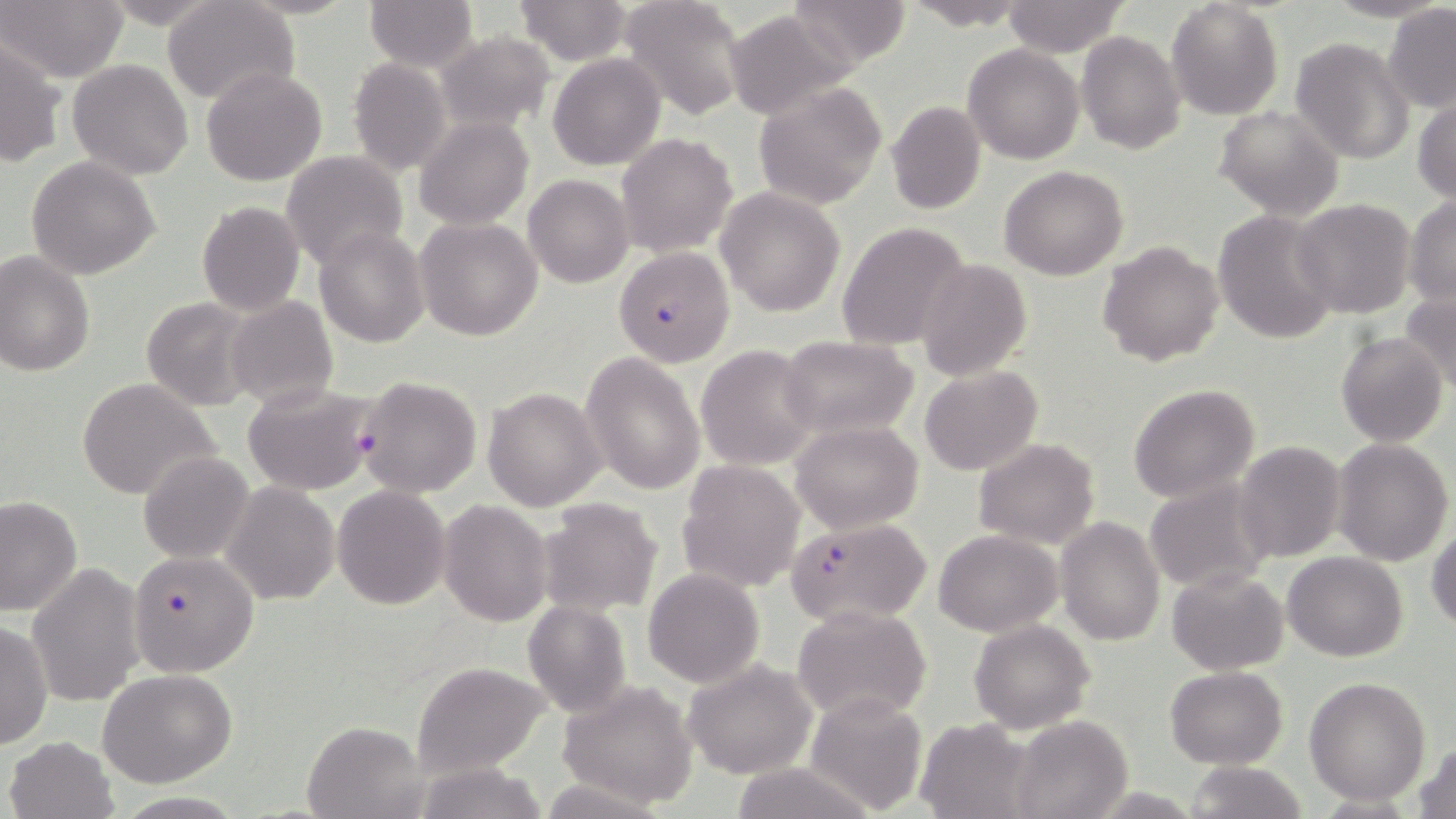

slide_level_diagnosis: Plasmodium falciparum
image_size: 1456×819 pixels
modality: optical microscopy
preparation: thin blood film
field_of_view: single
magnification: 1000x
plasmodium_falciparum_infected_red_blood_cell_locations: 'approximate bounding boxes as (x1,y1)-(x2,y2) corner pairs in pixels: (614,247)-(735,367), (357,375)-(484,498), (785,518)-(933,626), (127,549)-(259,677)'
stain: May-Grünwald-Giemsa
uninfected_red_blood_cell_locations: 'approximate bounding boxes as (x1,y1)-(x2,y2) corner pairs in pixels: (3,0)-(129,83), (98,0)-(225,28), (365,0)-(478,71), (620,0)-(748,120), (785,0)-(914,67), (901,0)-(1036,29), (163,1)-(297,106), (515,1)-(633,65), (1001,1)-(1130,56), (1166,2)-(1284,119), (1383,4)-(1456,111), (722,9)-(855,120), (1078,30)-(1187,155), (433,31)-(556,133), (2,35)-(67,169), (1290,37)-(1415,167), (962,45)-(1083,165), (547,54)-(666,170), (347,56)-(451,177), (67,59)-(193,179), (201,66)-(326,185), (754,82)-(887,210), (1413,93)-(1456,202), (885,101)-(986,216), (1215,104)-(1346,221), (414,116)-(534,231), (617,133)-(738,259), (281,151)-(408,270), (27,157)-(163,279), (999,165)-(1129,280), (523,174)-(633,288), (716,187)-(845,317), (1404,195)-(1456,308), (1292,200)-(1415,317), (196,204)-(303,316), (1212,208)-(1341,345), (414,217)-(543,340), (837,222)-(971,353), (314,226)-(428,348), (1097,241)-(1225,368), (0,250)-(96,376), (917,258)-(1031,382), (1399,290)-(1456,393), (225,295)-(338,410), (142,297)-(257,411), (1335,330)-(1448,447), (780,336)-(918,440), (697,344)-(820,471), (581,352)-(706,495), (919,365)-(1041,477), (76,377)-(221,500), (241,381)-(381,496), (1128,383)-(1259,503), (483,385)-(606,512), (792,420)-(922,532), (974,437)-(1098,549), (1234,438)-(1347,562), (1333,439)-(1453,568), (138,449)-(254,563), (677,460)-(805,593), (1140,476)-(1277,595), (223,483)-(339,604), (332,485)-(451,609), (537,496)-(663,617), (0,497)-(83,619), (439,499)-(552,626), (1056,517)-(1166,645), (1427,527)-(1456,632), (935,529)-(1060,636), (1282,550)-(1408,661), (29,563)-(146,709), (642,567)-(765,689), (1166,569)-(1289,674), (523,602)-(630,716), (793,605)-(933,724), (969,618)-(1093,734), (1,620)-(52,752), (683,656)-(819,780), (411,661)-(550,775), (1165,666)-(1287,768), (100,670)-(238,786), (1305,676)-(1430,804), (558,680)-(699,809), (802,693)-(927,814), (1011,715)-(1133,819), (912,718)-(1039,818), (304,720)-(426,818), (4,736)-(117,818), (1414,739)-(1456,819), (1185,759)-(1309,818)'